Assess this cell for malaria.
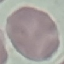
It is uninfected.

Cell patch, automatically extracted from a larger field of view and resized to 64 × 64 pixels. Giemsa-stained preparation. Thin smear of blood. Photographed with a smartphone camera at the microscope eyepiece.